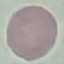

Malaria status: uninfected. Thin blood smear. Photographed with a smartphone camera at the microscope eyepiece. Giemsa-stained preparation. Automatically extracted cell patch, resized to 64 × 64 pixels.